Assess this cell for malaria.
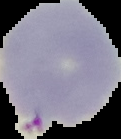

Uninfected.

The area outside the segmented cell region is set to black. Image is 121×139 pixels. From a thin blood film.